Classify this cell by malaria status.
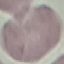

Uninfected.

{
  "preparation": "thin blood film",
  "capture": "smartphone camera at the microscope eyepiece",
  "image_type": "automatically extracted cell patch, resized to 64 × 64 pixels",
  "stain": "Giemsa"
}